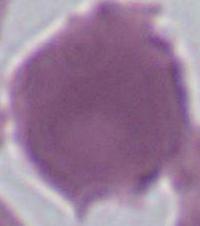
{
  "modality": "micrograph",
  "magnification": "400x or 1000x",
  "identification": "Plasmodium"
}